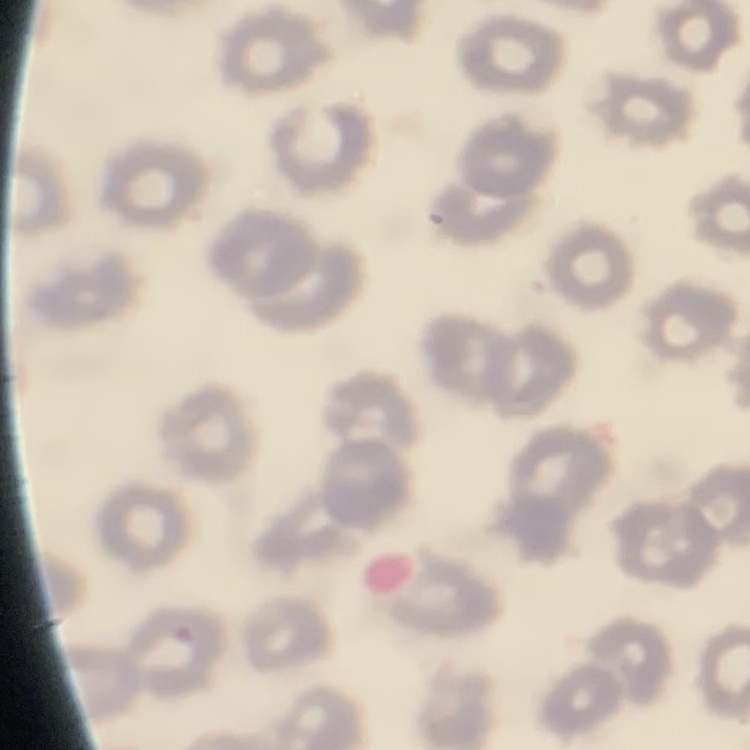

Summary:
  - Red blood cell morphology: no rouleaux formation
  - Stain: Field's or Giemsa
  - Image type: square crop of a larger photomicrograph
  - Preparation: thin blood smear